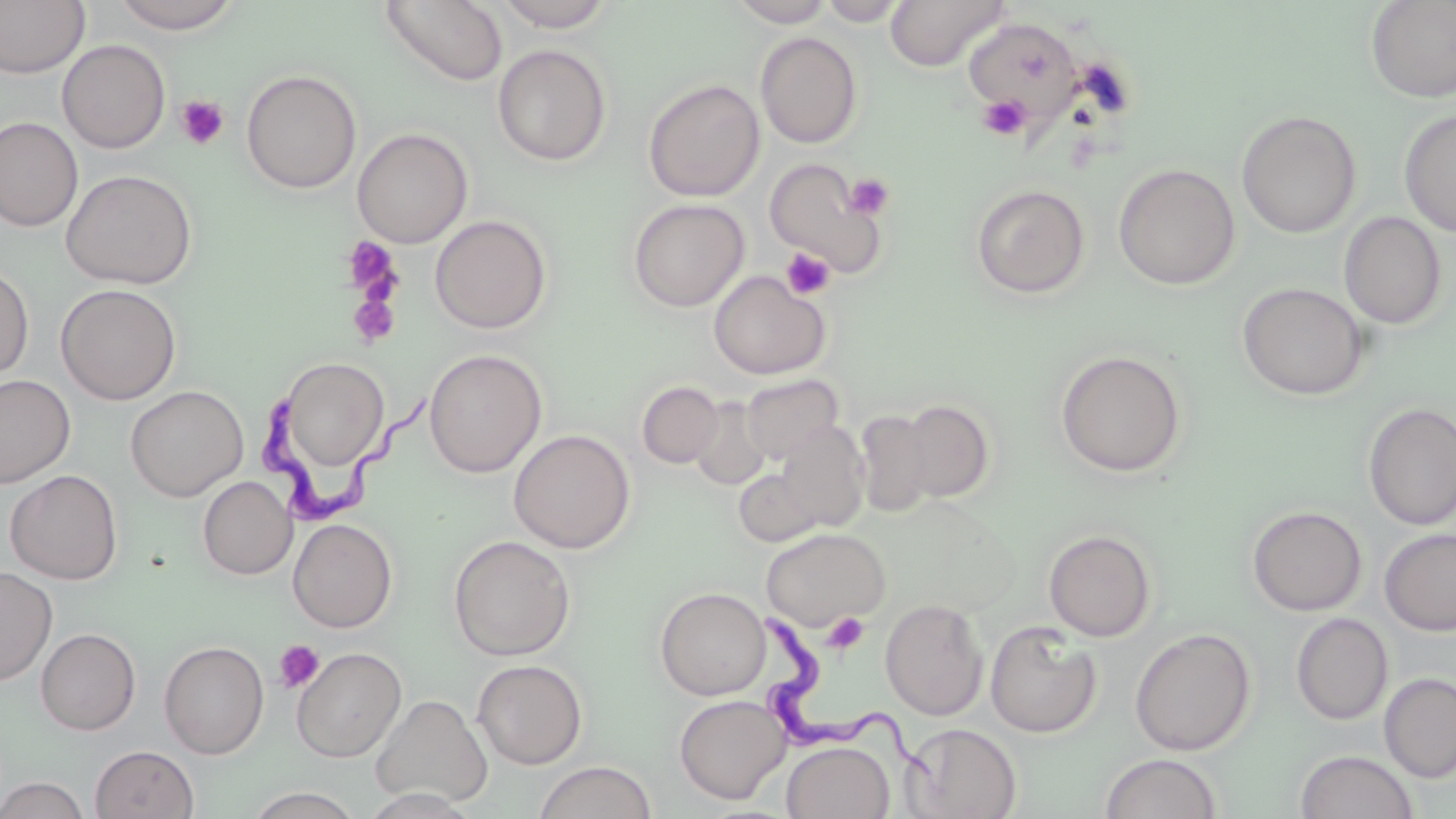

slide-level diagnosis = Trypanosoma brucei
image size = 1456×819 pixels
Trypanosoma brucei locations = approximate bounding boxes as (x1,y1)-(x2,y2) corner pairs in pixels: (256,381)-(438,530), (752,619)-(940,776)
field of view = single
uninfected red blood cell locations = approximate bounding boxes as (x1,y1)-(x2,y2) corner pairs in pixels: (0,0)-(90,78), (379,0)-(508,86), (494,0)-(618,32), (728,0)-(836,27), (885,0)-(1010,72), (110,1)-(244,34), (816,1)-(912,26), (1365,1)-(1456,103), (962,16)-(1083,123), (755,31)-(863,149), (57,40)-(171,153), (492,44)-(612,166), (241,69)-(361,194), (642,78)-(765,201), (1399,109)-(1456,237), (1236,110)-(1361,238), (0,117)-(83,232), (352,127)-(473,248), (763,157)-(890,279), (1113,163)-(1240,290), (60,169)-(198,289), (970,184)-(1090,300), (627,198)-(750,312), (1338,211)-(1448,329), (430,214)-(552,334), (0,263)-(34,382), (708,270)-(831,380), (1238,282)-(1369,400), (56,283)-(181,405), (424,349)-(547,477), (1055,349)-(1187,477), (274,357)-(390,477), (0,373)-(76,488), (741,374)-(843,464), (637,381)-(724,468), (125,385)-(248,501), (688,397)-(772,490), (897,399)-(995,502), (1362,402)-(1456,531), (854,410)-(935,517), (775,421)-(870,531), (508,429)-(635,554), (733,468)-(823,547), (4,469)-(124,584), (198,476)-(297,580), (1247,505)-(1366,616), (288,518)-(398,632), (761,527)-(890,629), (1379,527)-(1456,637), (1043,529)-(1157,642), (448,535)-(576,661), (0,566)-(58,686), (654,586)-(771,700), (880,598)-(988,720), (1291,613)-(1394,725), (984,621)-(1103,738), (36,627)-(141,735), (1130,627)-(1256,756), (159,640)-(270,759), (291,646)-(407,762), (472,659)-(588,769), (1378,673)-(1456,783), (370,693)-(493,809), (674,694)-(791,804), (899,723)-(1022,819), (781,740)-(895,819), (90,744)-(199,819), (1295,749)-(1418,819), (1099,752)-(1223,819), (533,761)-(658,819), (0,776)-(90,819), (246,787)-(365,818)
preparation = thin blood smear
modality = light microscopy
magnification = 1000x
platelet locations = approximate bounding boxes as (x1,y1)-(x2,y2) corner pairs in pixels: (175,95)-(230,150), (978,95)-(1030,141), (844,173)-(895,220), (341,236)-(402,299), (781,248)-(836,299), (347,294)-(401,347), (821,613)-(869,654), (274,639)-(325,693)
stain = May-Grünwald-Giemsa